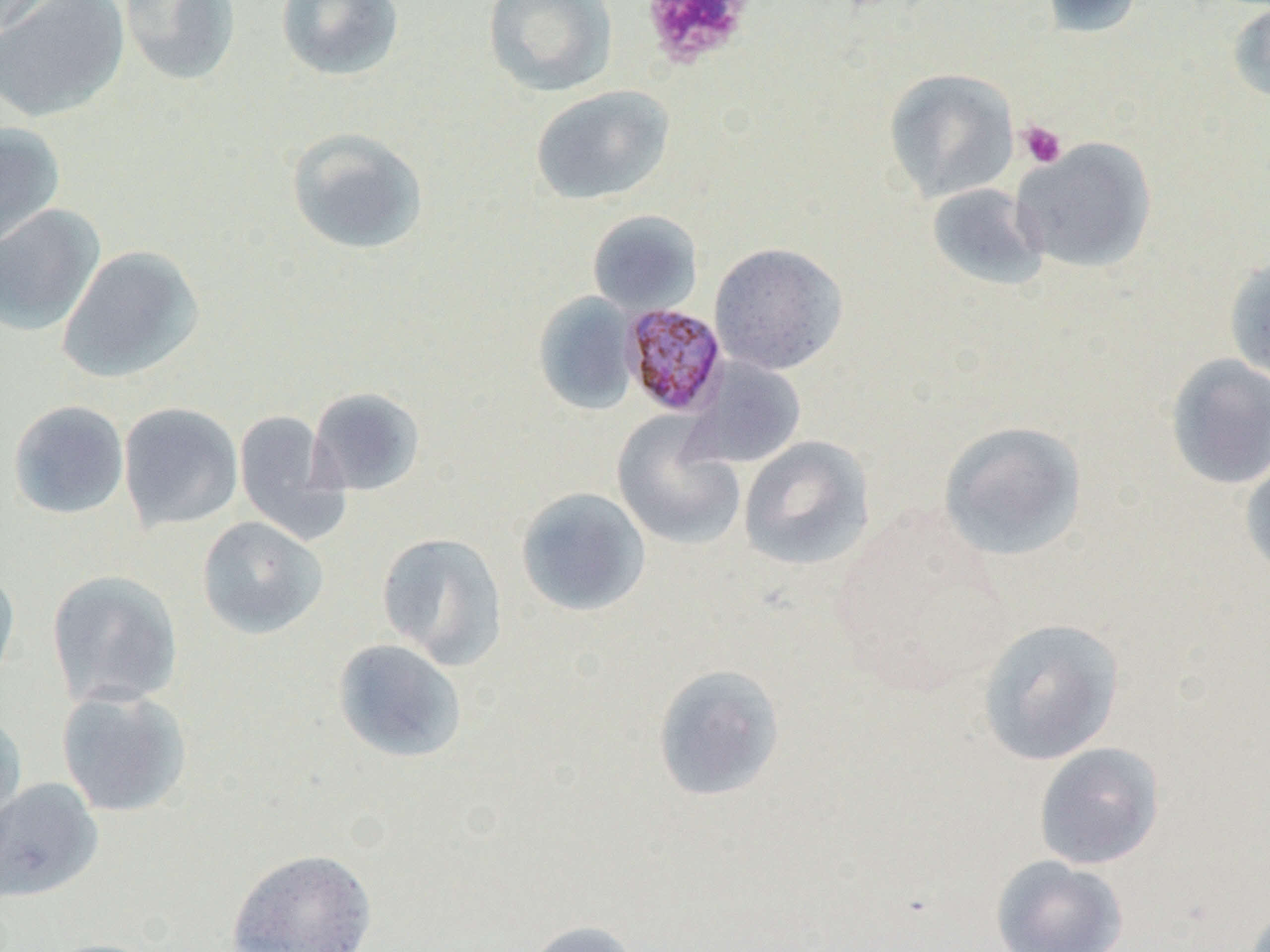
Approximate bounding boxes as (x1,y1)-(x2,y2) corner pairs in pixels. Platelet locations: (640,0)-(754,68), (1018,121)-(1067,169). Plasmodium malariae-infected red blood cell locations: (620,302)-(730,418). Uninfected red blood cell locations: (0,0)-(69,39), (0,0)-(130,123), (119,0)-(241,85), (275,0)-(405,82), (483,0)-(618,97), (1040,0)-(1144,38), (1227,3)-(1270,104), (883,68)-(1020,202), (530,85)-(674,205), (0,122)-(66,253), (285,127)-(429,256), (1012,137)-(1157,274), (926,182)-(1050,292), (0,203)-(105,336), (587,210)-(703,316), (708,242)-(848,376), (57,245)-(206,384), (1224,253)-(1270,388), (532,292)-(639,415), (1164,354)-(1270,490), (683,356)-(807,469), (307,387)-(426,496), (7,400)-(130,520), (118,402)-(243,531), (233,410)-(349,544), (611,413)-(745,551), (938,421)-(1087,562), (738,435)-(874,572), (1239,453)-(1270,583), (515,487)-(651,617), (197,516)-(329,639), (377,531)-(509,669), (0,564)-(21,692), (46,569)-(183,709), (976,618)-(1125,766), (332,638)-(467,764), (652,663)-(786,802), (56,686)-(193,817), (0,707)-(27,843), (1033,742)-(1164,870), (0,778)-(103,902), (226,848)-(378,952), (991,854)-(1128,952), (523,919)-(641,952), (39,938)-(167,952). Slide-level diagnosis: Plasmodium malariae. Thin blood smear. Optical microscopy. One field of a larger specimen. Image is 1270×952 pixels. 1000x magnification.